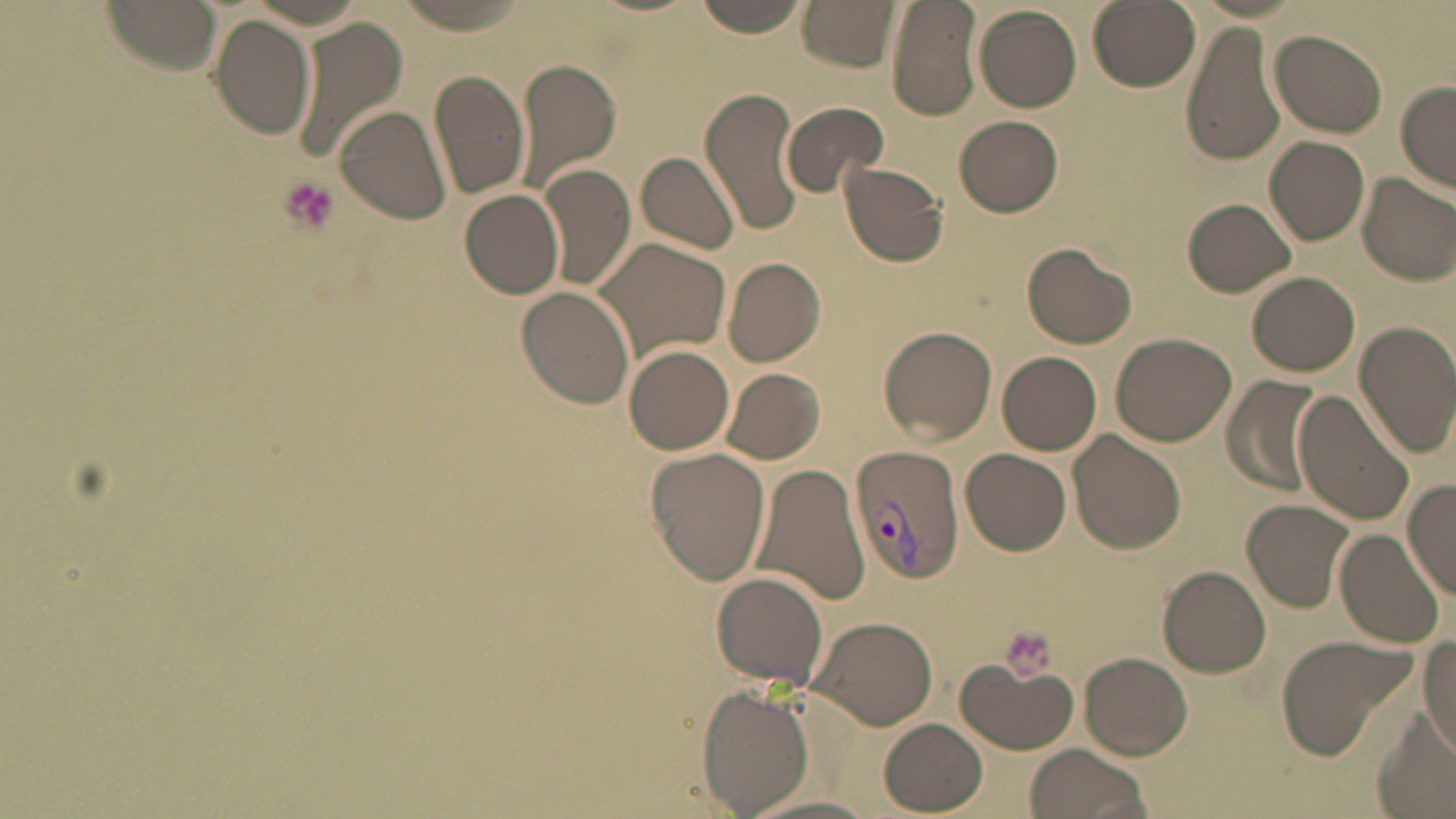 Approximate bounding boxes as (x1,y1)-(x2,y2) corner pairs in pixels. Plasmodium vivax-infected red blood cell locations: (847,445)-(964,585). Platelet locations: (276,177)-(339,234), (997,627)-(1056,683). Uninfected red blood cell locations: (102,0)-(224,73), (390,0)-(539,33), (691,0)-(812,38), (798,0)-(902,71), (886,0)-(983,120), (1087,0)-(1200,91), (974,5)-(1082,113), (209,15)-(315,138), (291,18)-(410,167), (1180,22)-(1286,166), (1270,31)-(1386,136), (515,59)-(622,190), (429,68)-(531,201), (1396,79)-(1456,191), (700,88)-(807,237), (780,101)-(888,196), (336,107)-(449,225), (955,114)-(1063,217), (1264,136)-(1370,246), (638,151)-(740,254), (838,161)-(949,268), (538,165)-(636,292), (1357,171)-(1456,287), (459,189)-(566,299), (1182,197)-(1296,297), (589,235)-(731,362), (1022,242)-(1137,349), (722,256)-(825,367), (1247,272)-(1359,378), (517,287)-(636,408), (1356,324)-(1454,454), (879,325)-(998,444), (1110,330)-(1238,445), (1327,342)-(1436,498), (623,344)-(735,454), (997,351)-(1102,454), (720,368)-(825,464), (1224,379)-(1325,493), (1292,386)-(1415,527), (1069,431)-(1186,553), (645,448)-(770,585), (961,449)-(1071,556), (751,462)-(872,608), (1402,479)-(1456,599), (1243,500)-(1353,614), (1335,525)-(1446,648), (1156,565)-(1271,677), (711,572)-(830,691), (810,615)-(936,730), (1274,633)-(1422,762), (1420,636)-(1456,756), (1080,653)-(1191,760), (956,658)-(1078,755), (698,685)-(813,817), (1373,716)-(1454,819), (879,718)-(988,814), (1023,744)-(1152,819), (743,795)-(886,819). Slide-level diagnosis: Plasmodium vivax. Image is 1456×819 pixels. May-Grünwald-Giemsa stain. One field of a larger specimen. Thin blood smear. 1000x magnification. Optical microscopy.